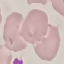

Result: negative for malaria parasites. Photographed with a smartphone camera at the microscope eyepiece. Thin smear of blood. Automatically extracted cell patch, resized to 64 × 64 pixels. Giemsa-stained preparation.